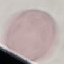
Summary:
  - Result: no malaria parasites detected
  - Capture: smartphone camera at the microscope eyepiece
  - Preparation: thin blood film
  - Stain: Giemsa
  - Image type: cell patch, automatically extracted from a larger field of view and resized to 64 × 64 pixels